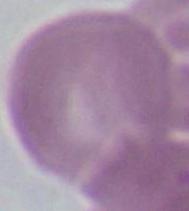
1000x magnification. Photomicrograph. A red blood cell is seen.